Report the malaria status of this cell.
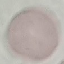

Uninfected.

Giemsa-stained preparation. Automatically extracted cell patch, resized to 64 × 64 pixels. Acquired by smartphone through the microscope eyepiece. Thin blood smear.